Identify the parasite.
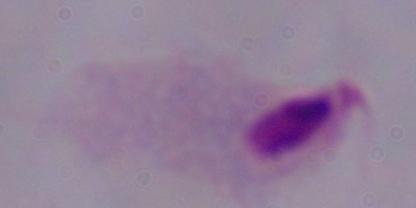

A trichomonad.

{
  "magnification": "1000x",
  "modality": "micrograph"
}